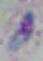
1000x magnification. Photomicrograph. Toxoplasma gondii is shown.